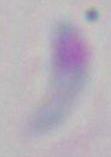 Photomicrograph. 1000x magnification. Toxoplasma gondii is shown.